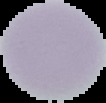

Image is 106×103 pixels. From a thin blood film. Result: negative for Plasmodium parasites. Cell region segmented out of the field of view; the surrounding area is masked to black.